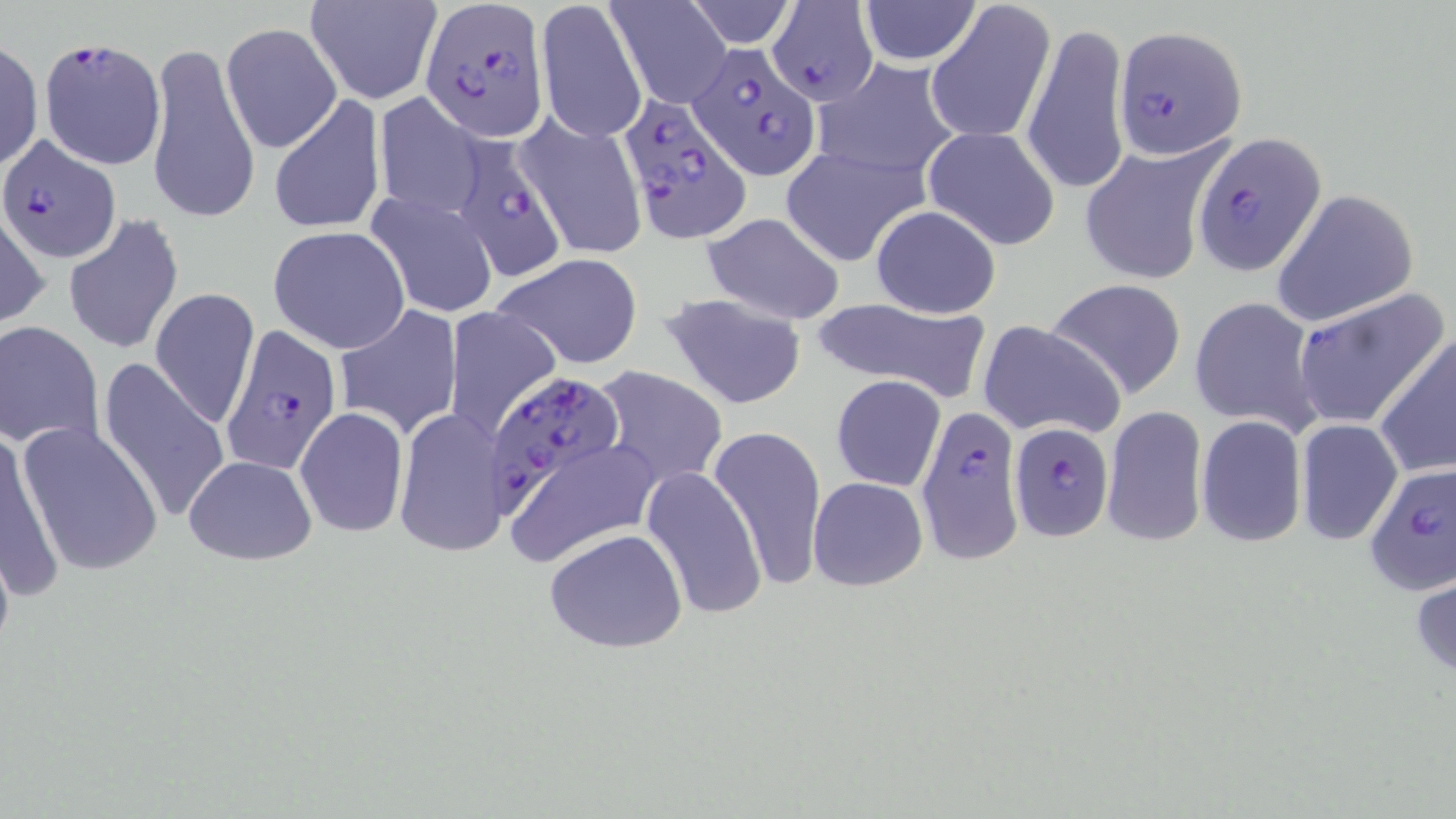
Summary:
  - Coordinate format: approximate bounding boxes as (x1,y1)-(x2,y2) corner pairs in pixels
  - Plasmodium falciparum-infected red blood cell locations: (422,2)-(550,140), (767,2)-(878,106), (1115,25)-(1247,159), (39,36)-(166,169), (689,41)-(817,176), (617,92)-(751,239), (462,129)-(564,287), (1193,131)-(1324,275), (1,135)-(119,261), (220,324)-(342,474), (487,373)-(625,510), (915,405)-(1021,566), (1009,418)-(1112,542), (1363,463)-(1456,595)
  - Uninfected red blood cell locations: (304,0)-(442,105), (535,0)-(646,144), (607,0)-(731,109), (684,0)-(800,48), (925,0)-(1056,147), (855,1)-(980,66), (1023,18)-(1129,201), (172,19)-(351,218), (222,22)-(342,152), (0,38)-(43,173), (145,39)-(259,226), (815,58)-(962,180), (267,92)-(387,237), (373,92)-(485,219), (515,112)-(649,259), (922,126)-(1060,250), (1080,143)-(1223,285), (780,146)-(926,267), (1270,189)-(1420,327), (365,192)-(501,319), (868,204)-(1002,319), (0,207)-(48,329), (699,213)-(846,325), (63,214)-(184,356), (268,226)-(410,353), (492,253)-(645,370), (1045,279)-(1190,400), (1295,287)-(1449,433), (150,288)-(261,432), (657,291)-(808,410), (1191,294)-(1323,435), (807,297)-(991,399), (333,304)-(463,440), (444,307)-(562,438), (977,320)-(1126,441), (0,322)-(104,450), (1375,332)-(1456,480), (99,357)-(230,526), (589,366)-(727,493), (830,375)-(946,492), (1102,405)-(1208,550), (296,406)-(409,536), (394,407)-(509,559), (1196,415)-(1306,547), (1296,419)-(1402,545), (16,420)-(163,578), (708,426)-(827,589), (1,428)-(62,602), (506,437)-(660,569), (184,455)-(315,564), (641,466)-(765,623), (808,476)-(928,591), (544,526)-(688,654), (1412,565)-(1456,682)
  - Slide-level diagnosis: Plasmodium falciparum
  - Field of view: one of a larger specimen
  - Image size: 1456×819 pixels
  - Stain: May-Grünwald-Giemsa
  - Modality: light microscopy
  - Preparation: thin blood film
  - Magnification: 1000x